State which parasite is depicted.
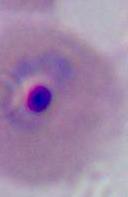
Plasmodium.

400x or 1000x magnification. Photomicrograph.